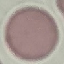

Malaria status: uninfected. Photographed with a smartphone camera at the microscope eyepiece. Cell patch, automatically extracted from a larger field of view and resized to 64 × 64 pixels. Thin blood smear. Giemsa stain.